Describe the morphology of the erythrocytes.
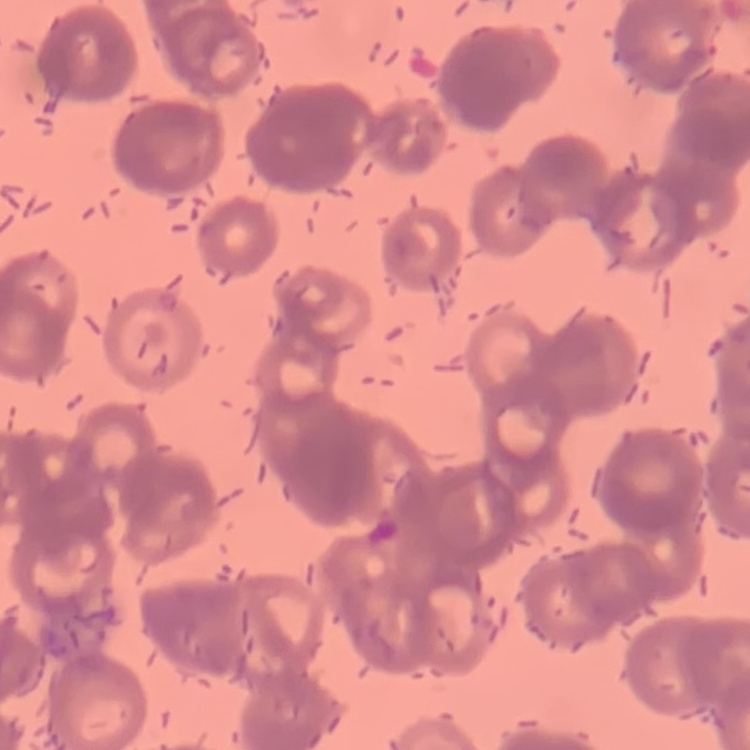
They show rouleaux formation.

Summary:
  - Image type: square crop of a larger photomicrograph
  - Preparation: thin blood smear
  - Stain: Field's or Giemsa